Evaluate for Plasmodium parasites.
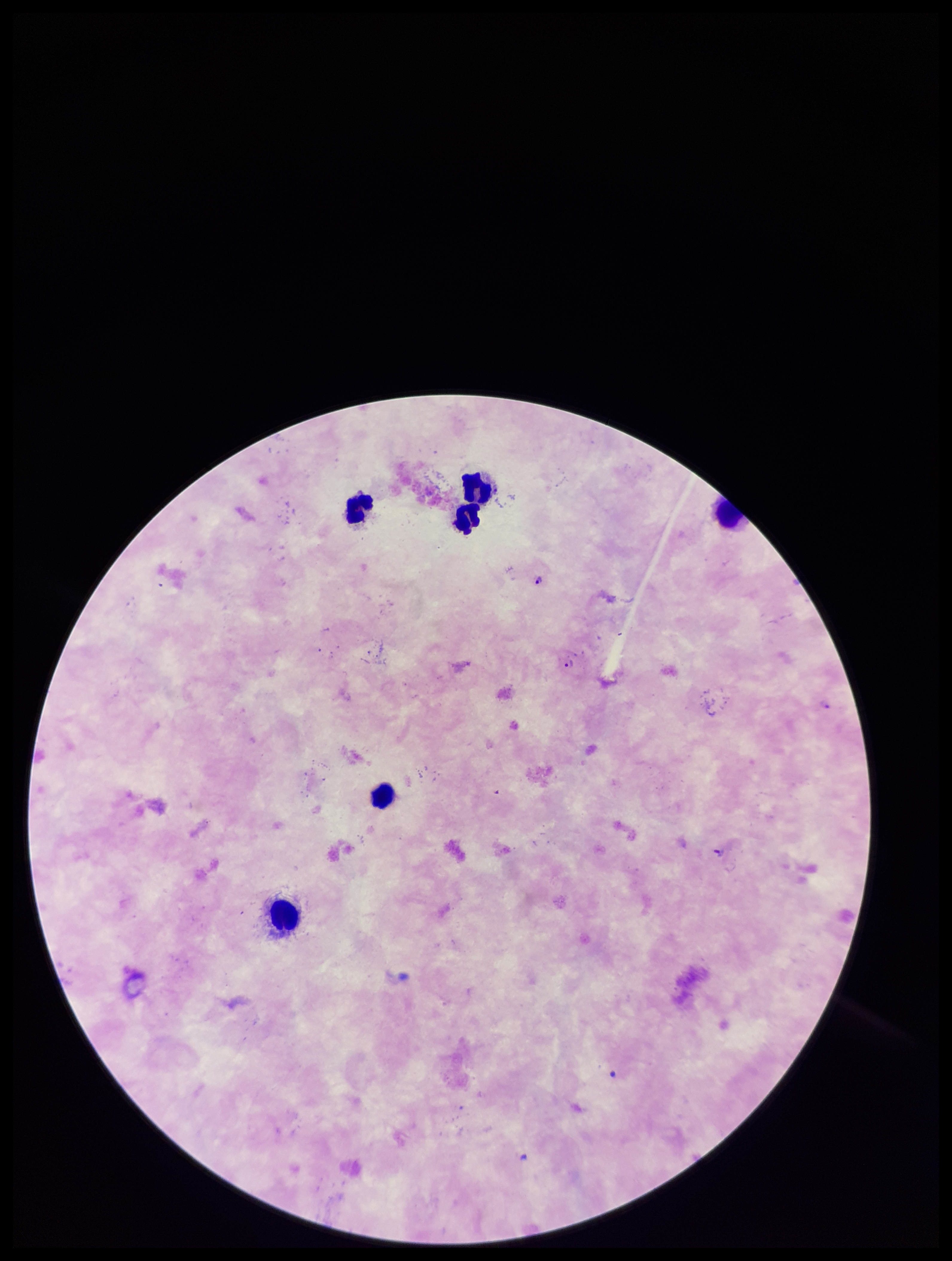

Identified.

Summary:
  - Patient malaria status: positive
  - Preparation: thick
  - Capture: smartphone photograph through the microscope eyepiece
  - Parasite count: 4
  - Field of view: single
  - Stain: Giemsa
  - Image size: 952×1261 pixels
  - Leukocyte count: 5
  - Species reported for this patient: Plasmodium falciparum